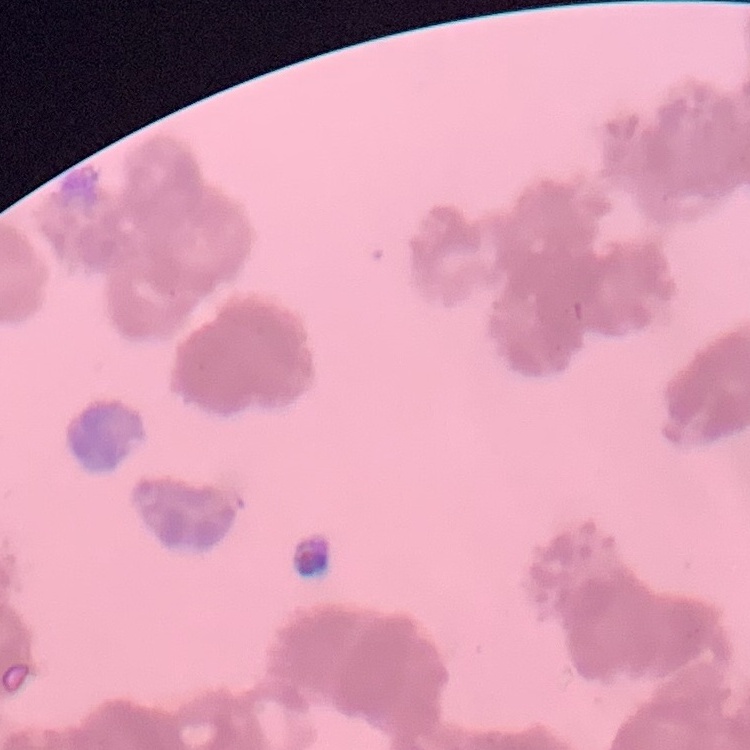

Summary:
  - Red blood cell morphology: rouleaux formation
  - Preparation: thin blood film
  - Stain: Field's or Giemsa
  - Image type: one tile cut from a larger photomicrograph